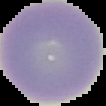

preparation = thin blood smear
image size = 106×106 pixels
malaria status = uninfected
image type = cell region segmented out of the field of view; surrounding area masked to black